Evaluate for malaria.
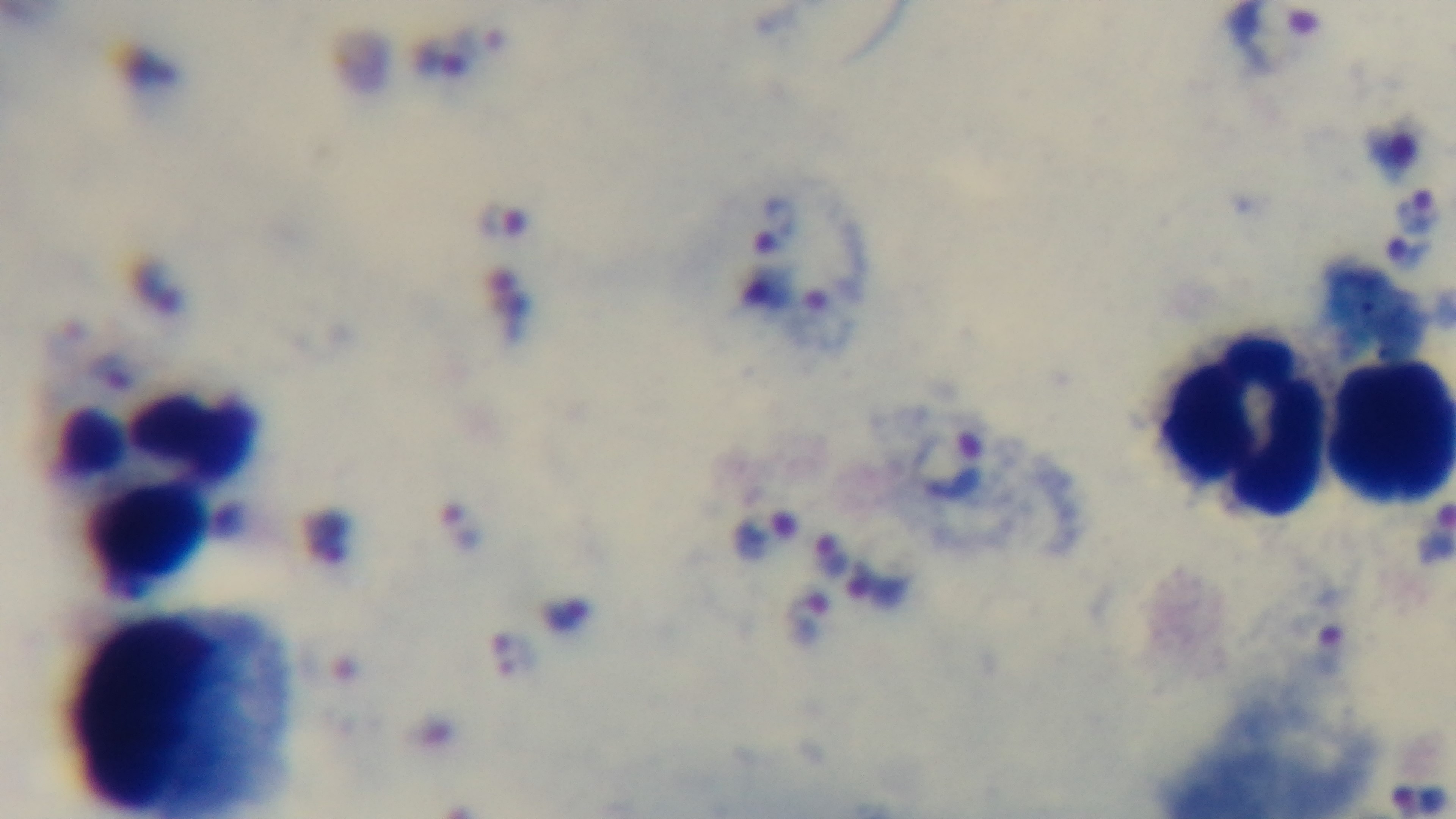
It is infected.

Photomicrograph. Oil-immersion objective, 100x. Single field of view. Giemsa stain. Mounted 4K digital camera. Preparation: thick blood film.